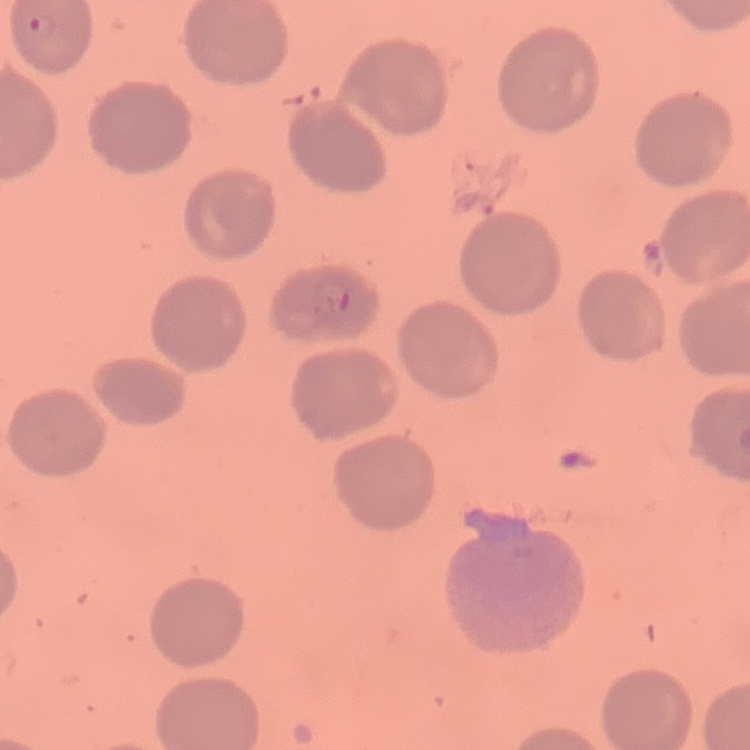

red_blood_cell_morphology: no rouleaux formation
image_type: one tile cut from a larger photomicrograph
preparation: thin blood film
stain: Field's or Giemsa